Name the cell type shown.
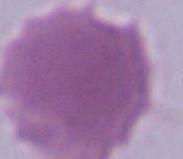

An erythrocyte.

Photomicrograph. 1000x magnification.